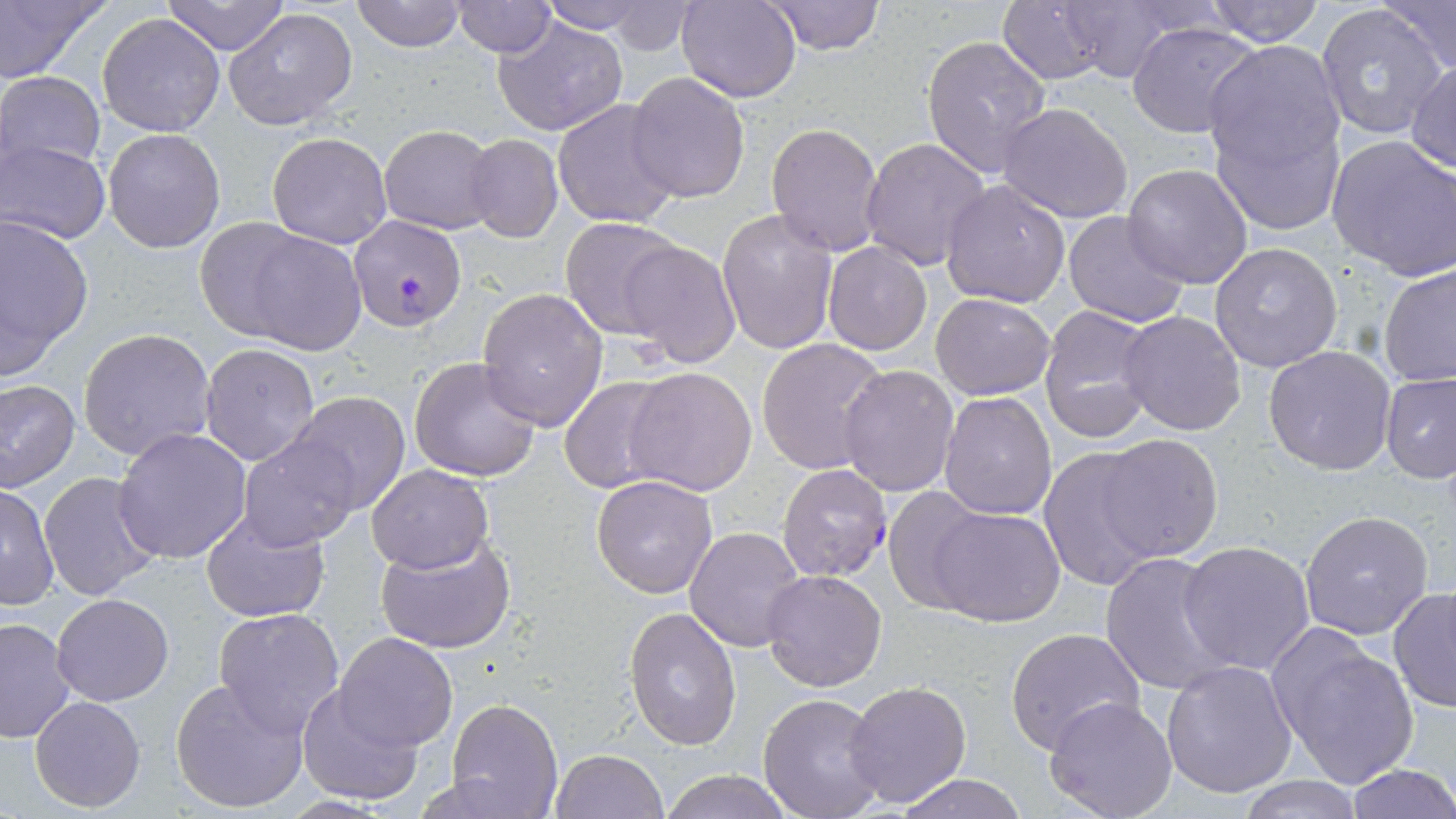

Summary:
  - Coordinate format: approximate bounding boxes as [x1, y1, x2, y2] in pixels
  - Plasmodium falciparum-infected red blood cell locations: [349, 213, 468, 331], [776, 463, 893, 583]
  - Uninfected red blood cell locations: [0, 0, 109, 86], [163, 0, 291, 55], [351, 0, 469, 52], [535, 0, 662, 35], [677, 0, 800, 102], [765, 0, 886, 55], [998, 0, 1110, 85], [1201, 0, 1328, 47], [1046, 1, 1196, 83], [1380, 1, 1455, 79], [451, 2, 557, 57], [1314, 4, 1448, 143], [223, 7, 358, 132], [96, 12, 226, 137], [492, 14, 629, 136], [1126, 21, 1263, 140], [920, 35, 1053, 182], [1204, 41, 1346, 176], [1408, 61, 1456, 175], [1, 72, 105, 178], [625, 73, 751, 203], [553, 99, 682, 230], [997, 103, 1134, 223], [1213, 112, 1346, 235], [767, 121, 886, 256], [380, 124, 497, 234], [102, 128, 225, 253], [267, 132, 391, 248], [1327, 133, 1456, 281], [464, 134, 562, 241], [860, 136, 990, 272], [2, 138, 110, 243], [1122, 163, 1253, 289], [939, 178, 1072, 309], [717, 208, 840, 356], [1062, 211, 1190, 329], [0, 213, 95, 379], [195, 217, 321, 339], [558, 217, 686, 338], [230, 225, 368, 355], [620, 238, 741, 369], [822, 241, 932, 356], [1210, 242, 1344, 374], [1378, 263, 1456, 389], [477, 287, 608, 431], [930, 292, 1055, 401], [1037, 305, 1158, 445], [1117, 310, 1247, 435], [79, 327, 216, 461], [756, 337, 891, 474], [200, 343, 320, 466], [1264, 346, 1396, 475], [409, 355, 544, 482], [838, 365, 960, 498], [624, 367, 758, 496], [1379, 371, 1456, 483], [559, 375, 677, 495], [0, 380, 80, 493], [938, 390, 1056, 520], [284, 392, 414, 515], [113, 428, 252, 564], [1096, 433, 1224, 560], [239, 435, 362, 551], [1036, 449, 1159, 586], [366, 464, 492, 573], [39, 471, 164, 600], [591, 475, 717, 598], [0, 483, 59, 611], [882, 487, 990, 613], [930, 506, 1067, 626], [200, 509, 330, 624], [1299, 509, 1435, 640], [684, 528, 806, 651], [372, 531, 521, 657], [1178, 538, 1316, 674], [1100, 550, 1236, 697], [761, 569, 887, 691], [1388, 584, 1456, 712], [51, 592, 173, 706], [624, 606, 743, 749], [212, 607, 345, 734], [0, 617, 77, 743], [1268, 625, 1419, 789], [1005, 627, 1147, 757], [334, 633, 457, 750], [1159, 658, 1299, 798], [171, 677, 310, 814], [842, 679, 973, 809], [296, 686, 422, 808], [756, 692, 888, 819], [29, 694, 146, 813], [1044, 695, 1179, 819], [446, 699, 563, 819], [552, 749, 667, 819], [1344, 764, 1456, 819], [659, 769, 794, 819], [893, 772, 1032, 818], [1236, 777, 1365, 818]
  - Slide-level diagnosis: Plasmodium falciparum
  - Preparation: thin blood film
  - Modality: optical microscopy
  - Field of view: single
  - Stain: May-Grünwald-Giemsa
  - Magnification: 1000x
  - Image size: 1456×819 pixels